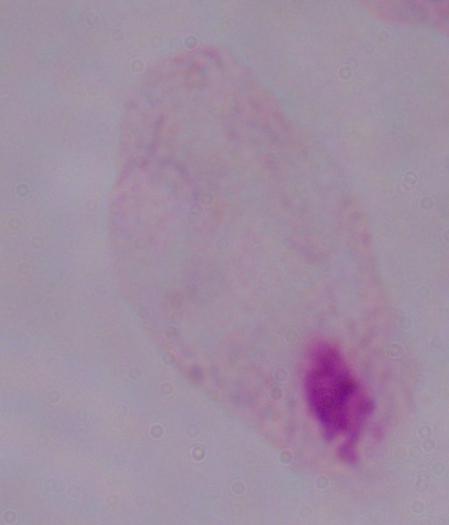

identification = trichomonad
magnification = 1000x
modality = photomicrograph